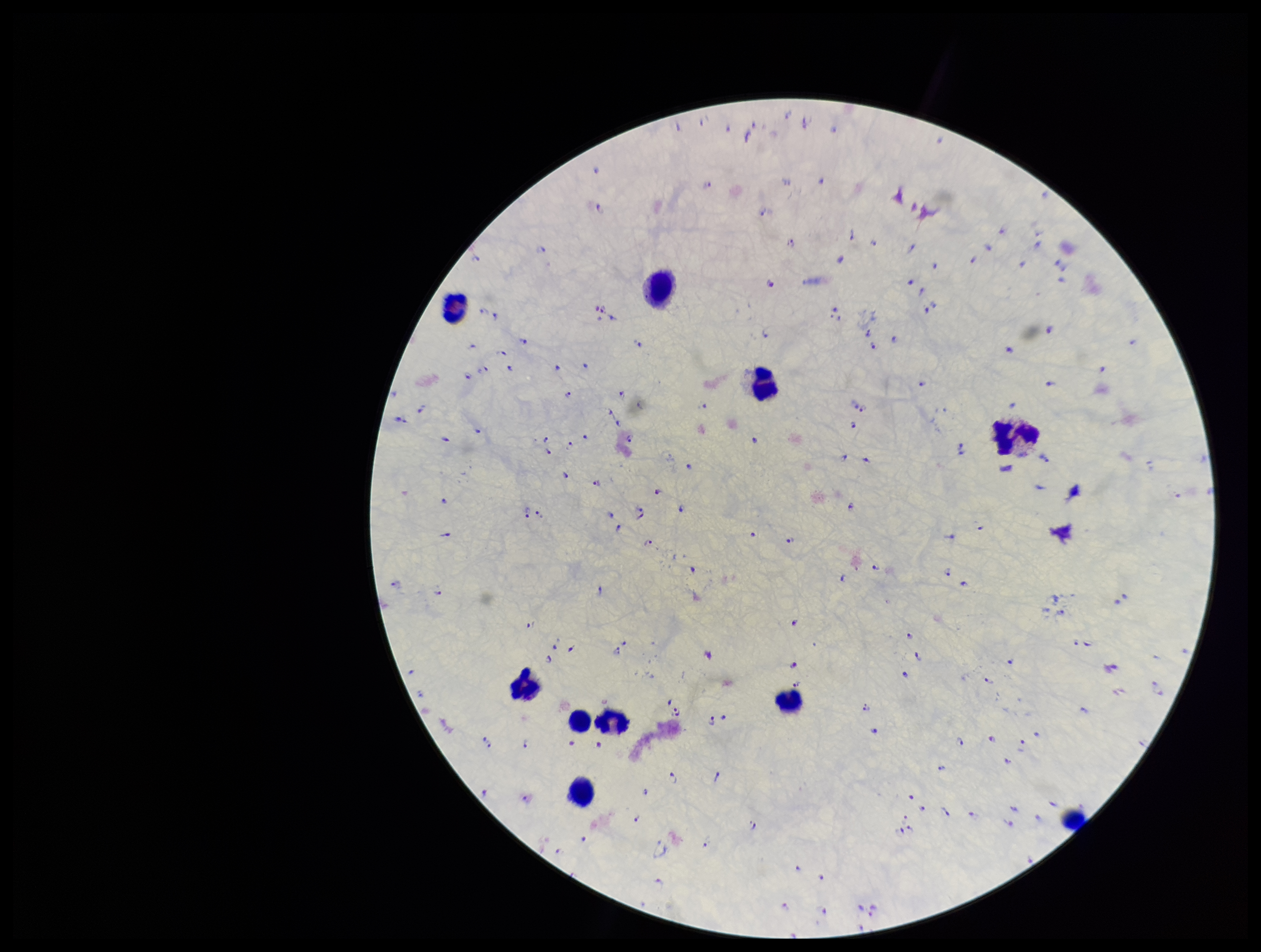 Patient malaria status: positive. Preparation: thick blood smear. Photographed through the microscope eyepiece with a smartphone camera. Leukocyte count: 10. Parasite count: 167. Plasmodium parasites: identified. Giemsa stain. One field from this slide. Species reported for this patient: Plasmodium falciparum. Image is 1261×952 pixels.